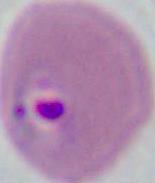
Summary:
  - Modality: micrograph
  - Magnification: 400x or 1000x
  - Identification: Plasmodium